Draw a bounding box around every artifact (platelet-like body, stain precipitate, or debris).
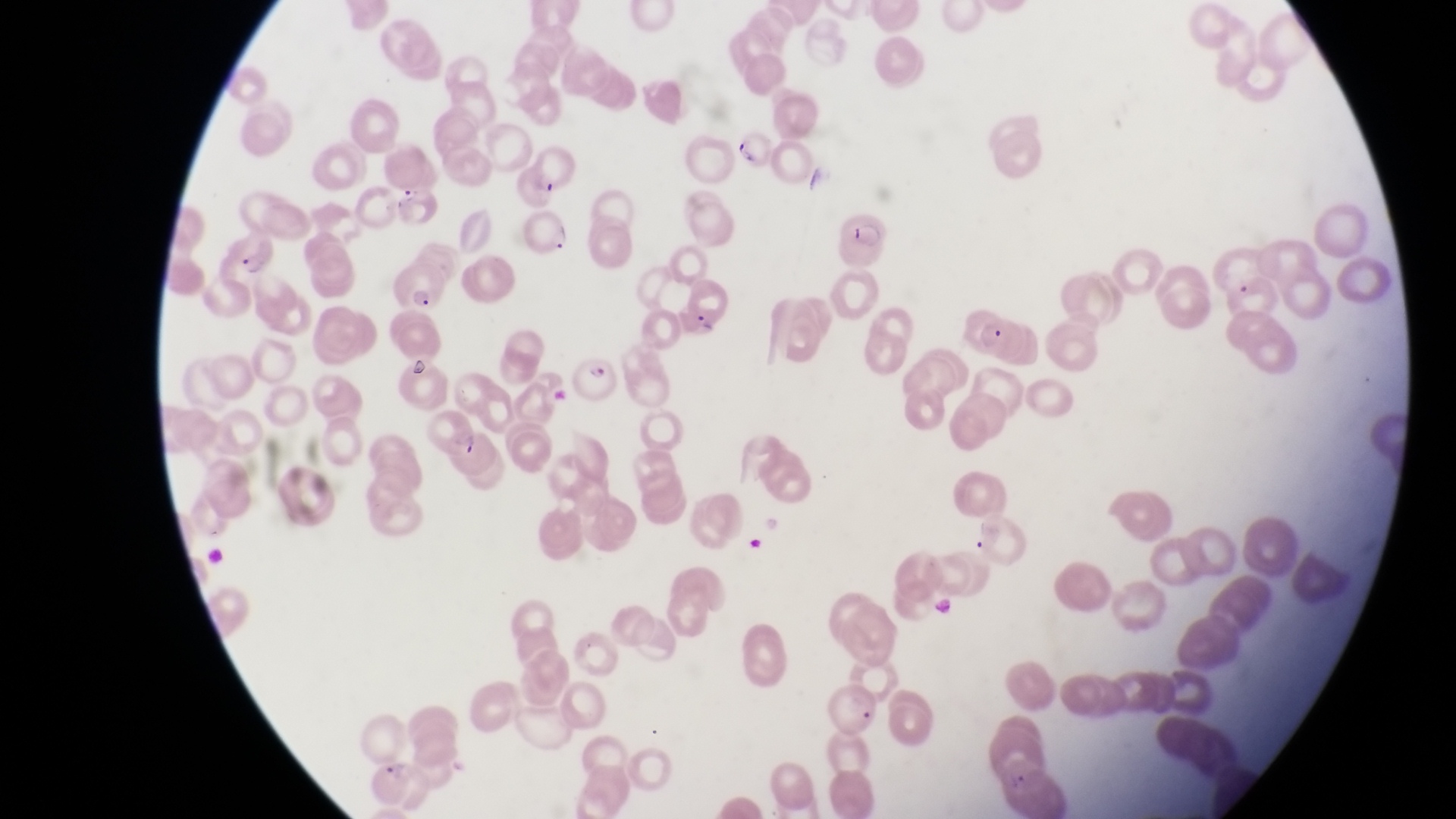
Approximate bounding boxes as left top right bottom in pixels.
Artifacts (platelet-like body, stain precipitate, or debris): 406 351 439 383.

{
  "parasitised_red_blood_cell_locations": "approximate bounding boxes as left top right bottom in pixels: 732 129 774 174; 391 184 437 230; 525 209 577 258; 835 209 895 265; 225 232 278 277; 394 262 443 311; 965 310 1012 359; 573 353 622 402",
  "magnification": "1000x",
  "capture": "smartphone photograph through the eyepiece of an Olympus CX-23 microscope",
  "field_of_view": "single",
  "preparation": "thin blood film",
  "image_size": "1456×819 pixels",
  "country": "Uganda"
}